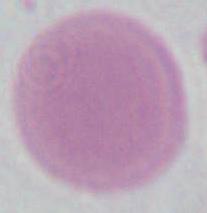 Micrograph. An erythrocyte is shown. 1000x magnification.